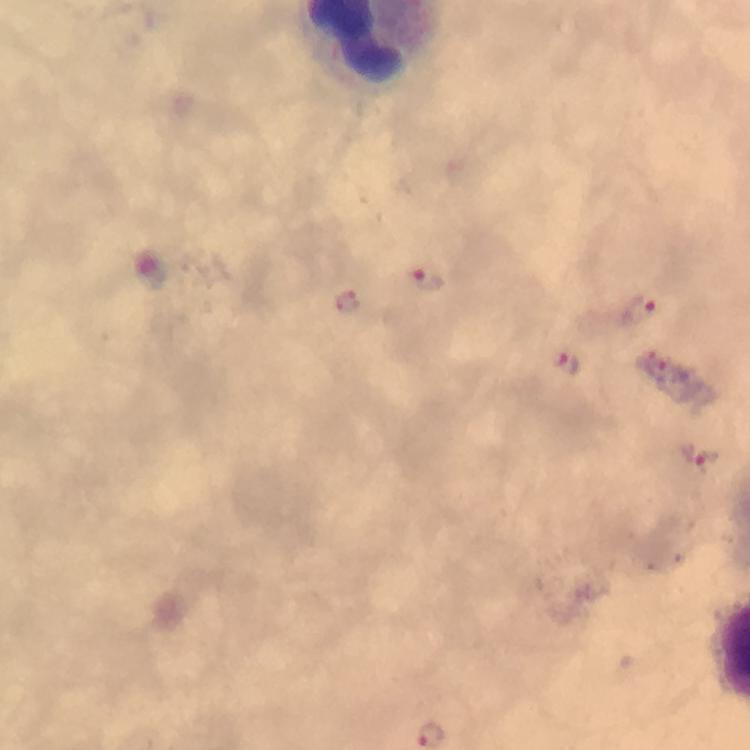

Approximate centers as {x, y} in pixels. Malaria parasite locations: {427, 278}, {347, 303}, {640, 311}, {564, 363}, {696, 457}. Thick blood smear. A crop from one field of view. 100x magnification. Giemsa-stained preparation. Immersion oil was used. From a diagnostic examination for malaria. Smartphone photograph taken through a microscope. Image is 750×750 pixels.